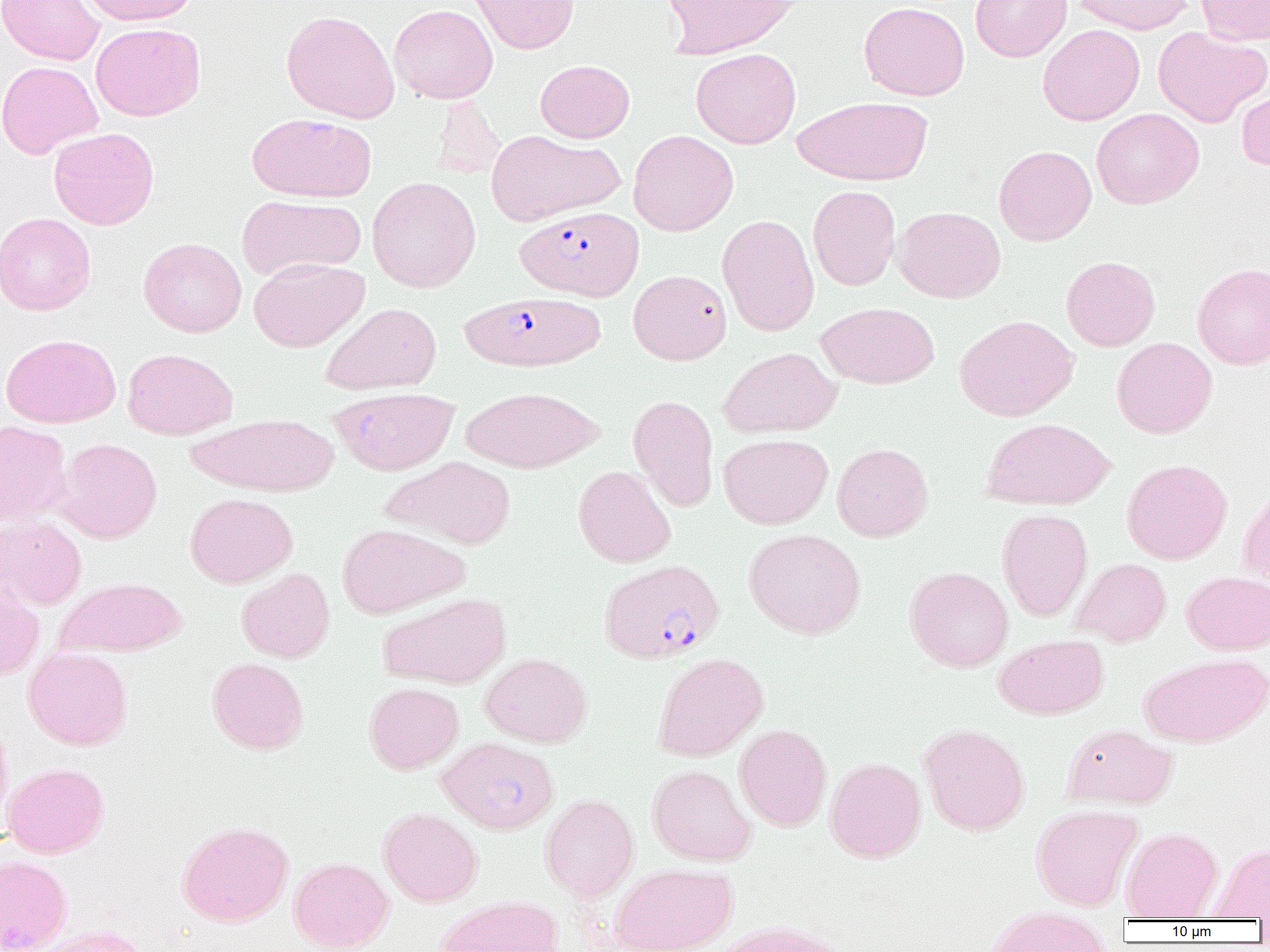

Summary:
  - Coordinate format: approximate bounding boxes as (x1,y1)-(x2,y2) corner pairs in pixels
  - Plasmodium falciparum-infected red blood cell locations: (516,205)-(644,301), (460,292)-(605,372), (600,559)-(724,664)
  - Uninfected red blood cell locations: (0,0)-(104,65), (81,0)-(198,26), (469,0)-(579,54), (663,0)-(797,59), (969,0)-(1072,62), (1070,0)-(1195,34), (1196,0)-(1270,45), (859,1)-(970,101), (389,4)-(498,104), (281,10)-(400,123), (91,22)-(205,121), (1037,24)-(1145,126), (1153,26)-(1269,127), (691,48)-(801,149), (535,59)-(634,143), (0,60)-(102,160), (1235,85)-(1270,171), (431,96)-(506,180), (792,96)-(933,186), (1092,108)-(1203,210), (247,113)-(377,202), (49,127)-(159,230), (628,129)-(738,236), (486,130)-(623,226), (994,145)-(1096,246), (367,176)-(480,293), (808,186)-(901,290), (236,195)-(366,281), (893,206)-(1005,303), (0,212)-(95,316), (717,214)-(819,336), (138,237)-(247,337), (1061,256)-(1160,351), (249,258)-(369,352), (1192,263)-(1270,370), (628,270)-(731,365), (816,301)-(939,389), (321,302)-(441,394), (954,314)-(1079,421), (1,334)-(120,428), (1112,337)-(1217,439), (719,347)-(841,438), (123,348)-(237,440), (461,386)-(603,474), (329,387)-(459,475), (628,395)-(719,511), (188,412)-(338,497), (981,418)-(1115,510), (0,420)-(72,527), (719,434)-(833,529), (55,438)-(162,544), (832,443)-(932,542), (384,456)-(516,549), (1121,459)-(1232,564), (574,465)-(676,567), (1238,481)-(1270,591), (185,493)-(297,588), (996,508)-(1092,621), (0,515)-(87,610), (337,523)-(470,618), (744,528)-(865,639), (1072,558)-(1171,647), (904,566)-(1013,672), (236,568)-(334,663), (1182,571)-(1270,654), (55,577)-(187,658), (0,578)-(45,682), (378,593)-(511,690), (994,633)-(1107,719), (23,646)-(132,751), (652,652)-(768,761), (1139,652)-(1269,747), (480,653)-(592,748), (206,657)-(309,754), (364,682)-(464,774), (0,713)-(13,833), (919,723)-(1030,836), (1062,723)-(1177,810), (734,724)-(832,831), (436,736)-(559,834), (825,757)-(926,863), (2,762)-(109,858), (647,764)-(756,866), (539,794)-(639,901), (1031,804)-(1142,911), (378,808)-(482,907), (177,820)-(294,927), (1121,827)-(1222,920), (1207,842)-(1270,920), (0,855)-(72,952), (289,857)-(394,952), (610,863)-(738,952), (436,896)-(564,952), (985,908)-(1113,952), (713,919)-(845,952), (29,924)-(151,952)
  - Slide-level diagnosis: Plasmodium falciparum
  - Image size: 1270×952 pixels
  - Magnification: 1000x
  - Preparation: thin blood film
  - Field of view: one of a larger specimen
  - Modality: light microscopy